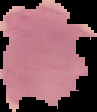

Summary:
  - Image size: 97×112 pixels
  - Image type: segmented cell region on a black background
  - Malaria status: parasitized
  - Preparation: thin blood smear